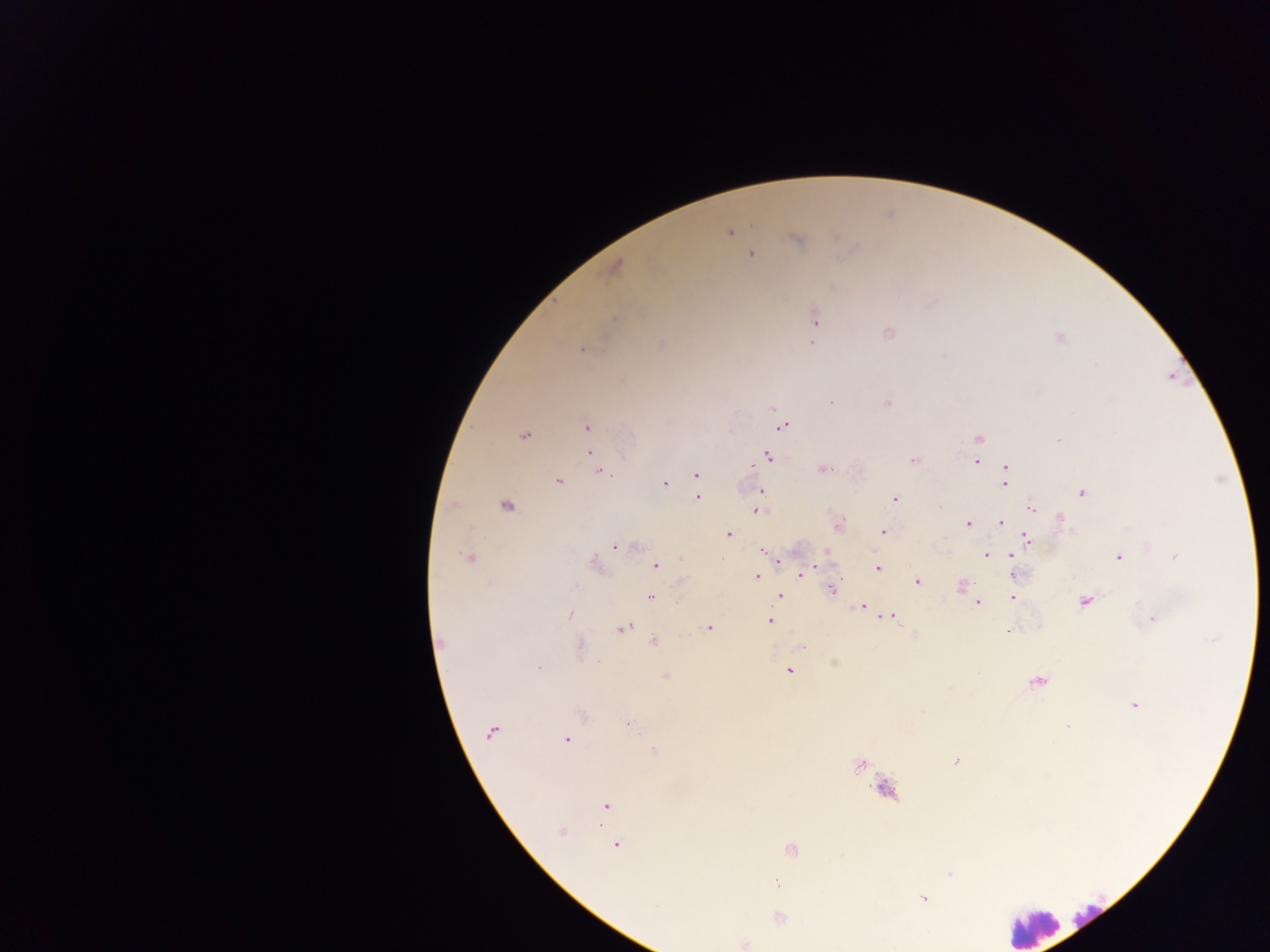
Approximate centers as x y in pixels. Leukocyte locations: 1033 926. Malaria parasite locations: 730 232; 836 237; 795 240; 751 254; 614 267; 832 287; 614 318; 815 319; 887 333; 1059 338; 811 343; 582 350; 831 402; 887 403; 773 408; 783 426; 587 427; 524 436; 979 438; 589 452; 768 456; 914 461; 976 462; 1006 466; 825 469; 600 472; 696 475; 558 481; 698 482; 665 483; 1005 483; 760 491; 1082 492; 697 498; 894 499; 505 505; 939 507; 1031 508; 758 509; 1059 517; 1001 522; 968 524; 839 525; 883 531; 728 534; 1026 538; 615 546; 1148 546; 827 554; 987 555; 1012 555; 1118 557; 1176 557; 469 558; 680 558; 722 560; 778 560; 596 563; 656 565; 878 568; 801 573; 1015 575; 755 577; 682 580; 918 581; 961 585; 831 590; 780 596; 650 597; 1012 598; 978 602; 1084 602; 858 607; 569 616; 888 616; 1154 620; 769 622; 623 628; 709 628; 1008 633; 914 636; 653 641; 440 642; 580 644; 801 647; 539 667; 789 671; 977 672; 665 675; 1037 681; 949 688; 1135 705; 582 716; 628 724; 1068 728; 491 732; 567 739; 654 751; 955 762; 859 766; 605 806; 561 831; 616 845; 791 850; 950 874; 775 883; 923 898; 656 905; 779 918; 745 944. Sample from Ghana. Mobile-phone photograph taken through the microscope. Single field of view. Thick blood smear. Image is 1270×952 pixels.